Classify this cell by malaria status.
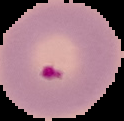

Parasitized.

preparation: thin blood smear
image_size: 124×121 pixels
image_type: cell region segmented out of the field of view; surrounding area masked to black